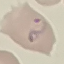

Summary:
  - Result: malaria parasites identified
  - Stain: Giemsa
  - Image type: cell patch, automatically extracted from a larger field of view and resized to 64 × 64 pixels
  - Capture: smartphone camera at the microscope eyepiece
  - Preparation: thin blood film